Outline each blood parasite and name the species.
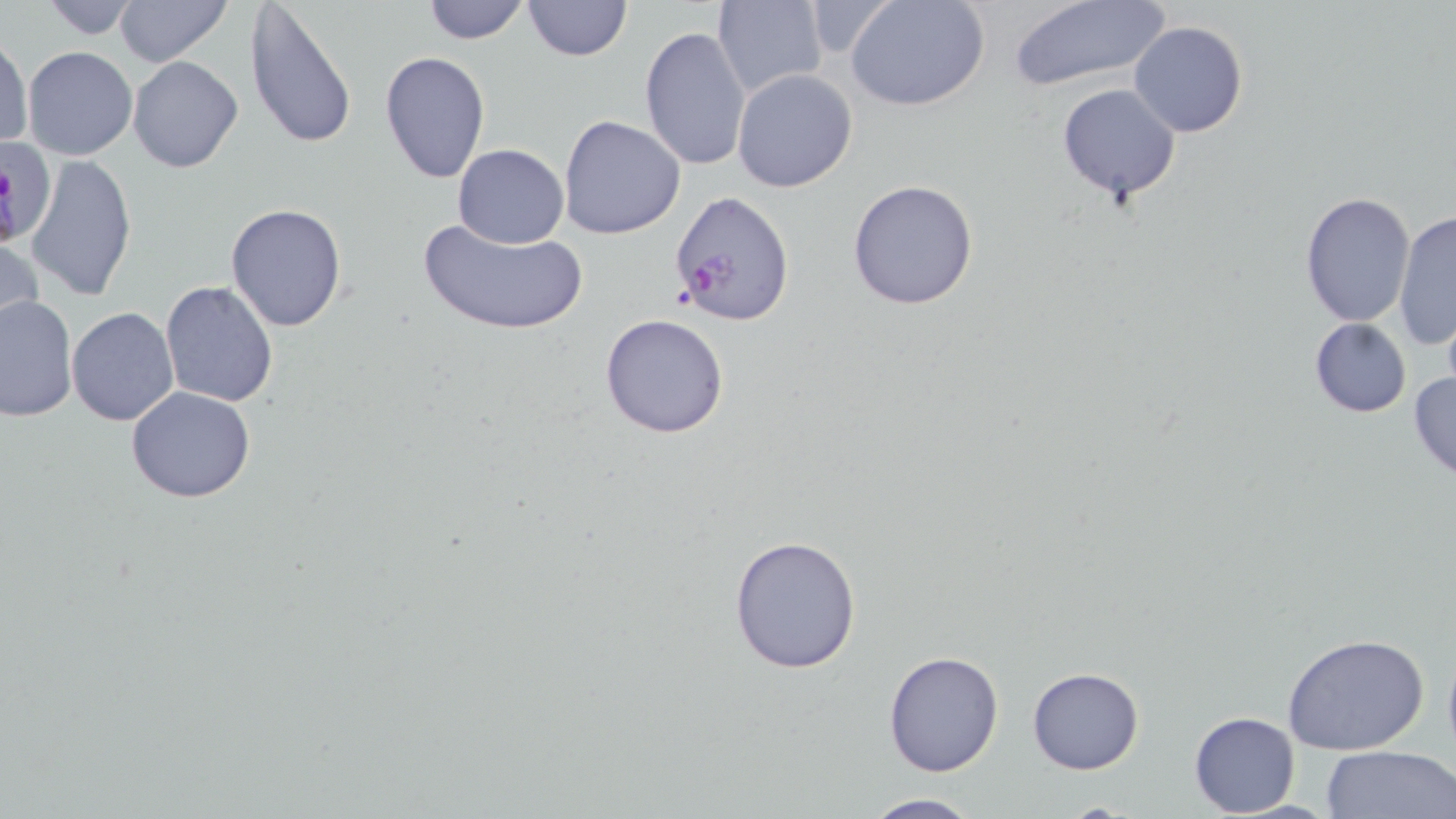
Approximate bounding boxes as [x1, y1, x2, y2] in pixels.
Plasmodium falciparum-infected red blood cells: [668, 190, 797, 326].
No Plasmodium ovale, Plasmodium malariae, Plasmodium vivax, Babesia divergens, or Trypanosoma brucei observed.

Summary:
  - Uninfected red blood cell locations: [35, 0, 148, 39], [421, 0, 531, 44], [523, 0, 632, 60], [713, 0, 829, 100], [846, 0, 990, 111], [1006, 0, 1172, 91], [113, 1, 231, 68], [244, 1, 358, 151], [1130, 21, 1248, 137], [639, 25, 751, 172], [0, 34, 33, 150], [22, 46, 138, 160], [379, 51, 491, 184], [128, 56, 244, 173], [732, 69, 858, 193], [1056, 83, 1180, 204], [558, 114, 687, 240], [452, 143, 570, 248], [26, 152, 137, 301], [846, 178, 980, 311], [1300, 192, 1416, 326], [225, 203, 348, 332], [1394, 209, 1456, 352], [417, 216, 587, 336], [0, 232, 44, 346], [159, 279, 279, 407], [0, 294, 77, 422], [66, 307, 179, 426], [599, 313, 731, 440], [1308, 318, 1412, 418], [1408, 369, 1456, 484], [125, 386, 257, 503], [728, 532, 863, 675], [1283, 635, 1429, 756], [882, 649, 1004, 777], [1027, 666, 1144, 774], [1188, 710, 1300, 816], [1318, 745, 1456, 819], [858, 793, 984, 819]
  - Slide-level diagnosis: Plasmodium falciparum
  - Stain: May-Grünwald-Giemsa
  - Image size: 1456×819 pixels
  - Preparation: thin blood film
  - Field of view: one of a larger specimen
  - Magnification: 1000x
  - Modality: light microscopy